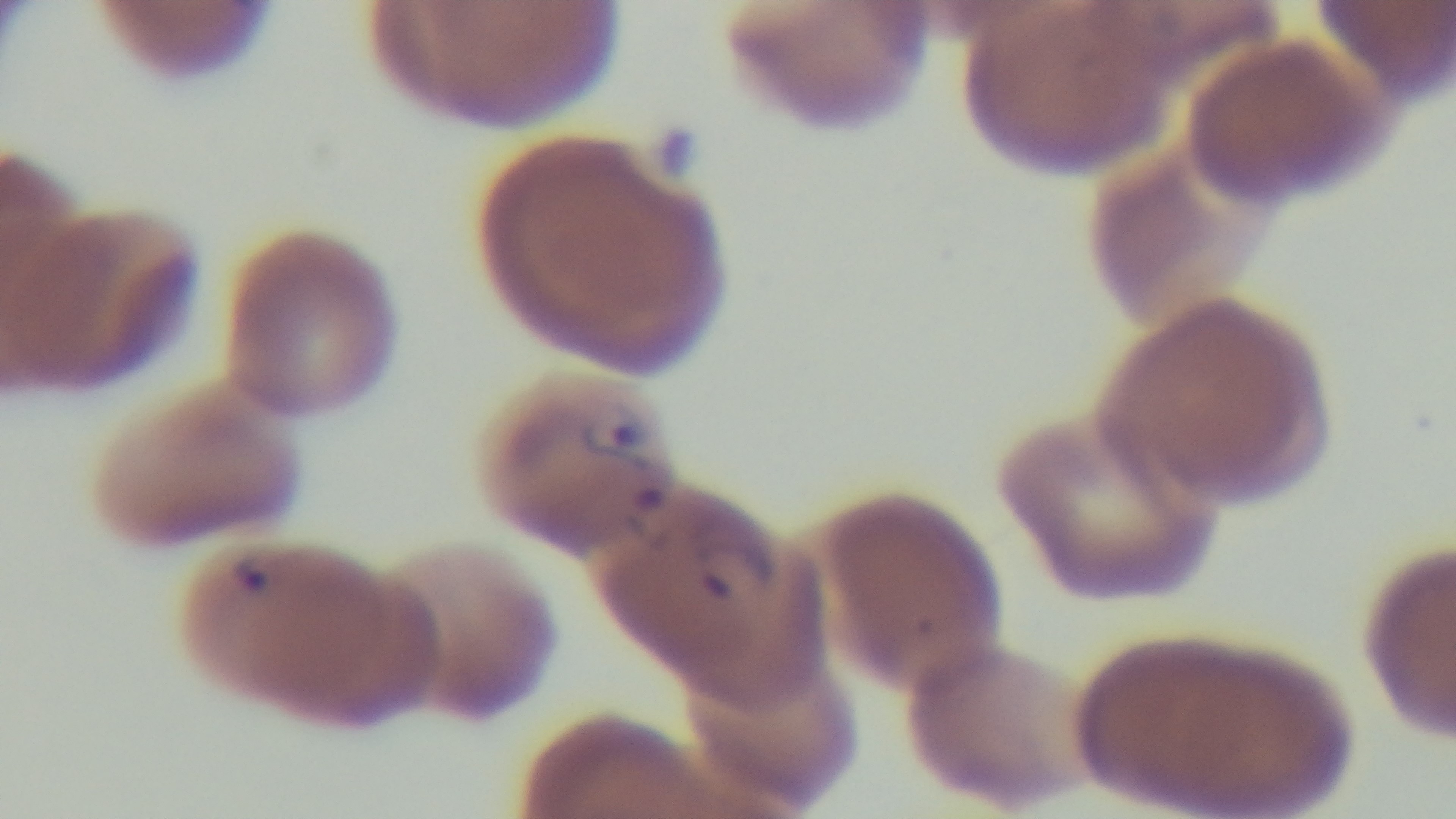
Malaria status: infected. One field from the slide. Giemsa-stained. 100x oil-immersion objective. Photomicrograph. Mounted 4K digital camera. Preparation: thin.